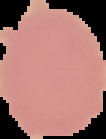
Summary:
  - Preparation: thin blood smear
  - Image size: 106×139 pixels
  - Image type: segmented cell region with the area outside set to black
  - Malaria status: uninfected